Outline each blood parasite and name the species.
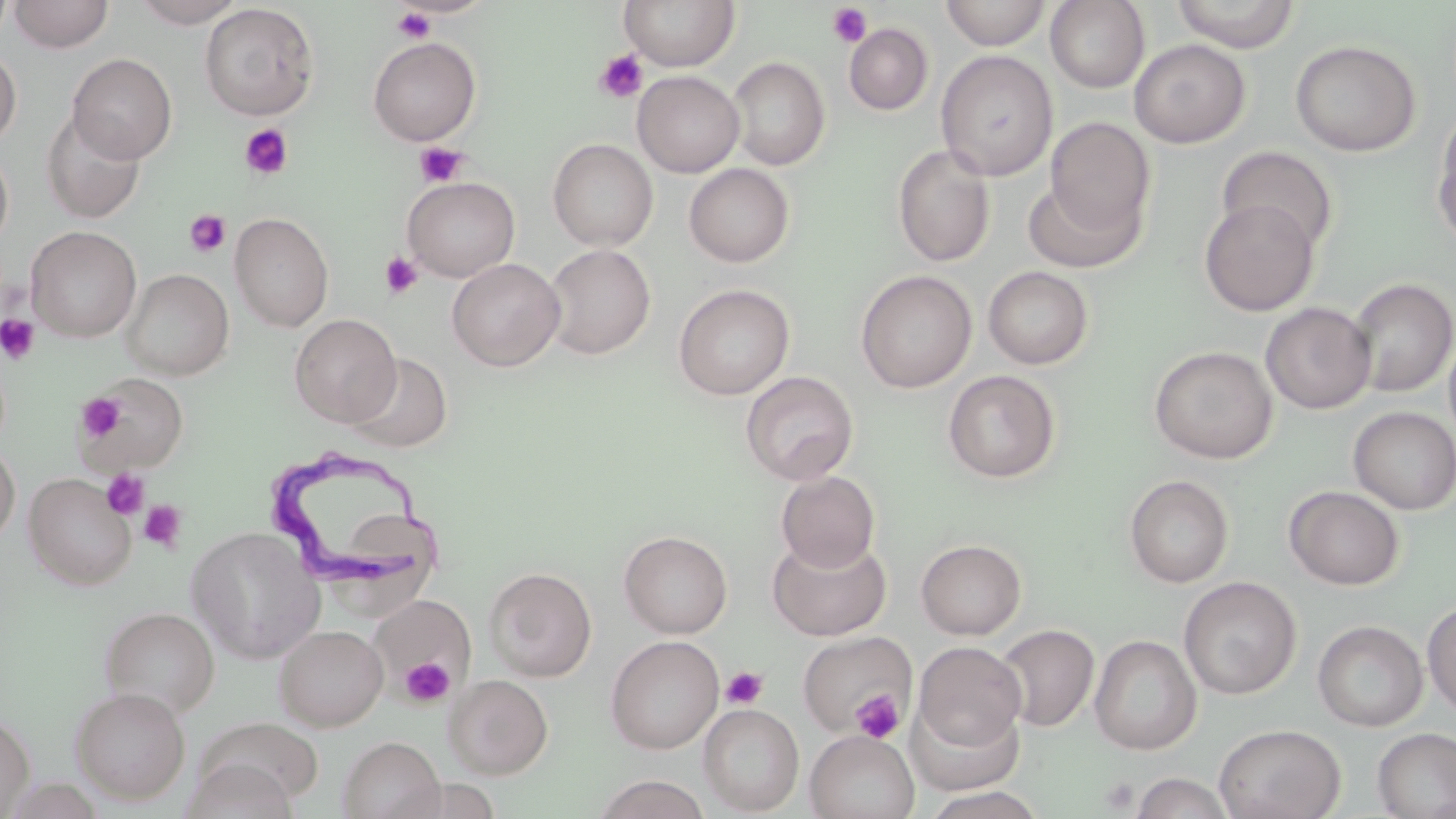
Approximate bounding boxes as named x1/y1/x2/y2 corners in pixels.
Trypanosoma brucei: (x1=265, y1=450, x2=452, y2=582).
No Plasmodium falciparum, Plasmodium ovale, Plasmodium malariae, Plasmodium vivax, or Babesia divergens observed.

slide-level diagnosis = Trypanosoma brucei
preparation = thin blood film
uninfected red blood cell locations = approximate bounding boxes as named x1/y1/x2/y2 corners in pixels: (x1=8, y1=0, x2=114, y2=52), (x1=130, y1=0, x2=247, y2=27), (x1=618, y1=0, x2=741, y2=71), (x1=940, y1=0, x2=1052, y2=50), (x1=1170, y1=0, x2=1300, y2=52), (x1=1045, y1=1, x2=1149, y2=92), (x1=199, y1=3, x2=319, y2=120), (x1=844, y1=22, x2=933, y2=115), (x1=367, y1=37, x2=482, y2=146), (x1=1129, y1=39, x2=1250, y2=148), (x1=1290, y1=39, x2=1420, y2=157), (x1=0, y1=48, x2=22, y2=148), (x1=935, y1=50, x2=1058, y2=181), (x1=67, y1=53, x2=177, y2=163), (x1=727, y1=57, x2=830, y2=170), (x1=632, y1=70, x2=744, y2=178), (x1=1432, y1=107, x2=1456, y2=249), (x1=41, y1=109, x2=146, y2=224), (x1=1044, y1=117, x2=1155, y2=239), (x1=548, y1=138, x2=658, y2=251), (x1=0, y1=144, x2=14, y2=253), (x1=892, y1=144, x2=996, y2=267), (x1=1216, y1=146, x2=1339, y2=254), (x1=684, y1=163, x2=795, y2=267), (x1=402, y1=177, x2=520, y2=281), (x1=1023, y1=179, x2=1145, y2=273), (x1=1199, y1=198, x2=1320, y2=316), (x1=230, y1=213, x2=334, y2=331), (x1=26, y1=226, x2=141, y2=342), (x1=544, y1=244, x2=656, y2=359), (x1=447, y1=258, x2=565, y2=371), (x1=982, y1=266, x2=1093, y2=369), (x1=121, y1=268, x2=234, y2=379), (x1=855, y1=270, x2=977, y2=393), (x1=1347, y1=277, x2=1456, y2=397), (x1=673, y1=283, x2=795, y2=399), (x1=1260, y1=302, x2=1376, y2=414), (x1=290, y1=313, x2=401, y2=426), (x1=1443, y1=326, x2=1456, y2=451), (x1=1149, y1=345, x2=1278, y2=463), (x1=345, y1=352, x2=453, y2=453), (x1=740, y1=370, x2=858, y2=485), (x1=942, y1=370, x2=1061, y2=483), (x1=84, y1=373, x2=189, y2=471), (x1=1349, y1=406, x2=1456, y2=514), (x1=0, y1=442, x2=20, y2=547), (x1=775, y1=471, x2=880, y2=572), (x1=23, y1=473, x2=137, y2=589), (x1=1124, y1=474, x2=1234, y2=588), (x1=1284, y1=486, x2=1405, y2=590), (x1=335, y1=515, x2=444, y2=616), (x1=186, y1=526, x2=325, y2=663), (x1=619, y1=530, x2=733, y2=638), (x1=767, y1=534, x2=891, y2=641), (x1=915, y1=538, x2=1026, y2=640), (x1=485, y1=566, x2=597, y2=681), (x1=1179, y1=576, x2=1302, y2=700), (x1=369, y1=593, x2=475, y2=699), (x1=1422, y1=599, x2=1456, y2=717), (x1=99, y1=606, x2=220, y2=718), (x1=1313, y1=620, x2=1428, y2=732), (x1=274, y1=624, x2=388, y2=731), (x1=995, y1=624, x2=1100, y2=732), (x1=797, y1=630, x2=915, y2=737), (x1=1089, y1=634, x2=1202, y2=754), (x1=606, y1=635, x2=724, y2=753), (x1=912, y1=641, x2=1027, y2=755), (x1=444, y1=674, x2=553, y2=778), (x1=69, y1=686, x2=191, y2=804), (x1=906, y1=695, x2=1026, y2=795), (x1=698, y1=703, x2=805, y2=815), (x1=0, y1=711, x2=35, y2=818), (x1=1214, y1=723, x2=1346, y2=819), (x1=1372, y1=727, x2=1456, y2=818), (x1=805, y1=730, x2=920, y2=819), (x1=338, y1=736, x2=444, y2=819), (x1=180, y1=757, x2=300, y2=819), (x1=1128, y1=771, x2=1236, y2=818), (x1=590, y1=775, x2=713, y2=819), (x1=920, y1=787, x2=1048, y2=819)
field of view = single
stain = May-Grünwald-Giemsa
image size = 1456×819 pixels
modality = light microscopy
magnification = 1000x
platelet locations = approximate bounding boxes as named x1/y1/x2/y2 corners in pixels: (x1=827, y1=3, x2=873, y2=48), (x1=391, y1=7, x2=436, y2=45), (x1=595, y1=50, x2=647, y2=102), (x1=239, y1=124, x2=294, y2=181), (x1=414, y1=142, x2=468, y2=188), (x1=183, y1=209, x2=231, y2=259), (x1=380, y1=251, x2=424, y2=298), (x1=0, y1=314, x2=40, y2=364), (x1=79, y1=394, x2=125, y2=442), (x1=101, y1=468, x2=150, y2=519), (x1=139, y1=500, x2=186, y2=553), (x1=399, y1=656, x2=454, y2=708), (x1=721, y1=666, x2=768, y2=710), (x1=849, y1=690, x2=905, y2=743), (x1=1100, y1=775, x2=1139, y2=813)